Classify this cell by malaria status.
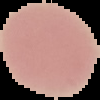

It is uninfected.

The area outside the segmented cell region is set to black. Image is 100×100 pixels. From a thin blood film.